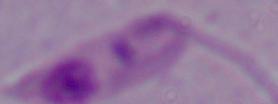
Summary:
  - Magnification: 1000x
  - Identification: Leishmania
  - Modality: micrograph